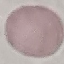
Summary:
  - Malaria status: uninfected
  - Preparation: thin blood film
  - Capture: smartphone camera at the microscope eyepiece
  - Stain: Giemsa
  - Image type: automatically extracted cell patch, resized to 64 × 64 pixels